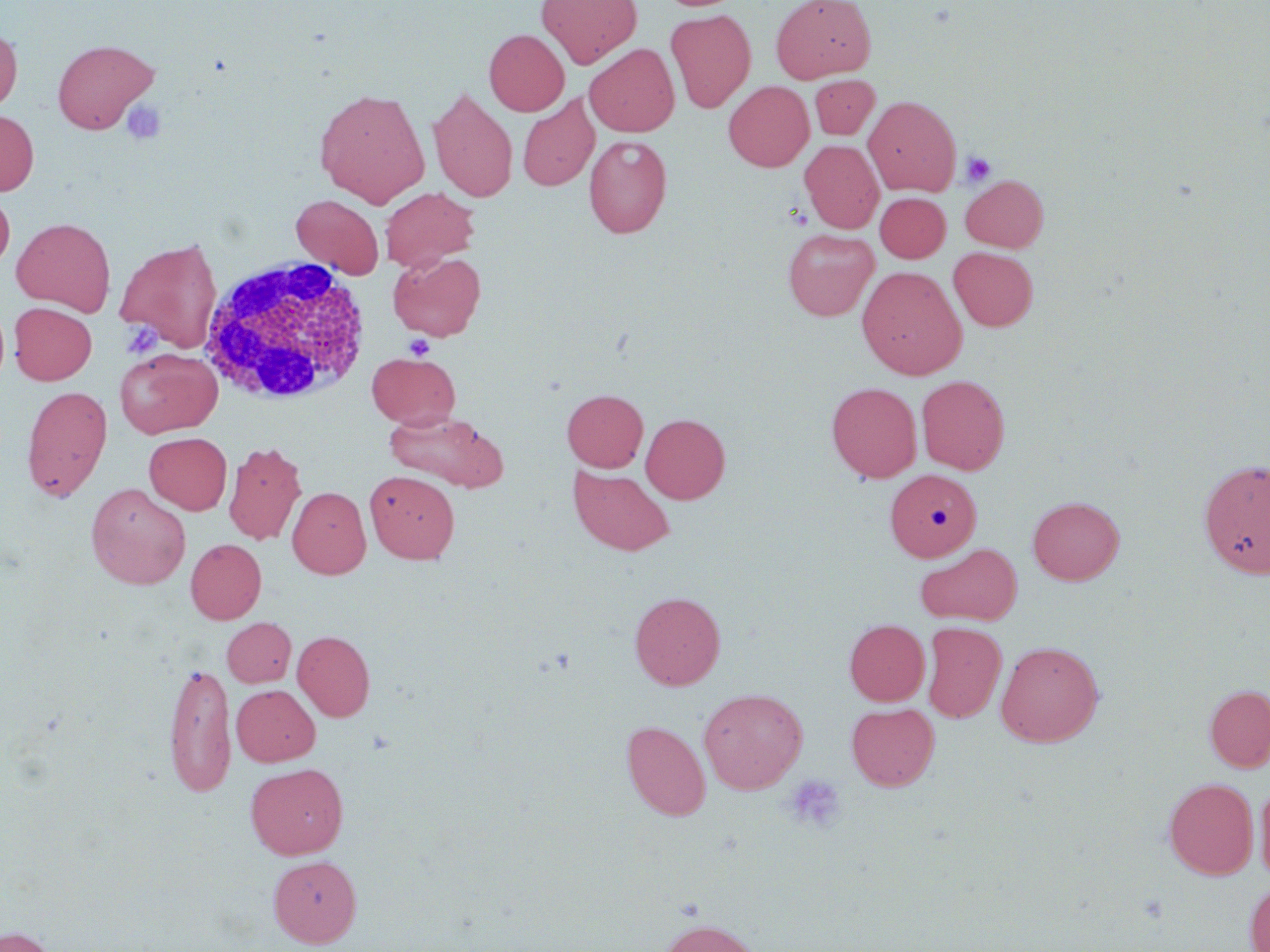
Approximate bounding boxes as (x1, y1, x2, y2) in pixels. White blood cell locations: (197, 256, 373, 405). Platelet locations: (121, 101, 166, 145), (960, 152, 996, 187), (121, 321, 163, 359), (405, 334, 434, 359), (786, 774, 846, 832). Uninfected red blood cell locations: (536, 0, 643, 68), (771, 0, 875, 83), (665, 8, 756, 113), (0, 27, 21, 115), (484, 29, 569, 116), (52, 38, 158, 134), (585, 44, 679, 136), (809, 75, 879, 139), (724, 81, 814, 171), (428, 86, 518, 202), (314, 88, 431, 207), (518, 95, 599, 191), (864, 95, 961, 196), (0, 109, 38, 196), (584, 134, 672, 238), (800, 140, 884, 233), (961, 175, 1048, 252), (380, 187, 479, 271), (0, 189, 14, 271), (875, 193, 950, 262), (291, 194, 384, 278), (12, 217, 115, 316), (783, 229, 879, 321), (115, 237, 223, 353), (949, 247, 1037, 331), (388, 251, 486, 341), (857, 266, 967, 380), (9, 302, 97, 384), (115, 348, 222, 438), (367, 352, 460, 429), (916, 375, 1010, 475), (827, 382, 922, 482), (21, 384, 112, 501), (562, 389, 647, 471), (383, 409, 508, 492), (641, 413, 730, 503), (144, 432, 232, 514), (223, 441, 307, 546), (1198, 458, 1270, 579), (568, 466, 674, 556), (885, 469, 981, 561), (365, 470, 459, 563), (86, 483, 190, 589), (287, 486, 370, 578), (1028, 496, 1124, 585), (186, 539, 266, 624), (916, 544, 1022, 625), (629, 591, 726, 689), (222, 617, 296, 687), (844, 619, 929, 706), (922, 621, 1006, 722), (292, 630, 375, 721), (996, 640, 1105, 747), (164, 659, 236, 797), (231, 685, 320, 766), (1204, 685, 1270, 772), (699, 688, 808, 793), (847, 703, 939, 791), (621, 720, 711, 821), (246, 763, 348, 859), (1164, 778, 1258, 879), (1254, 779, 1270, 884), (268, 856, 362, 947), (1244, 881, 1270, 952), (657, 918, 762, 952), (1, 926, 57, 952). Slide-level diagnosis: negative for blood parasites. Single field of view. May-Grünwald-Giemsa-stained preparation. Light microscopy. Image is 1270×952 pixels. Thin blood film. 1000x magnification.